Classify the preparation.
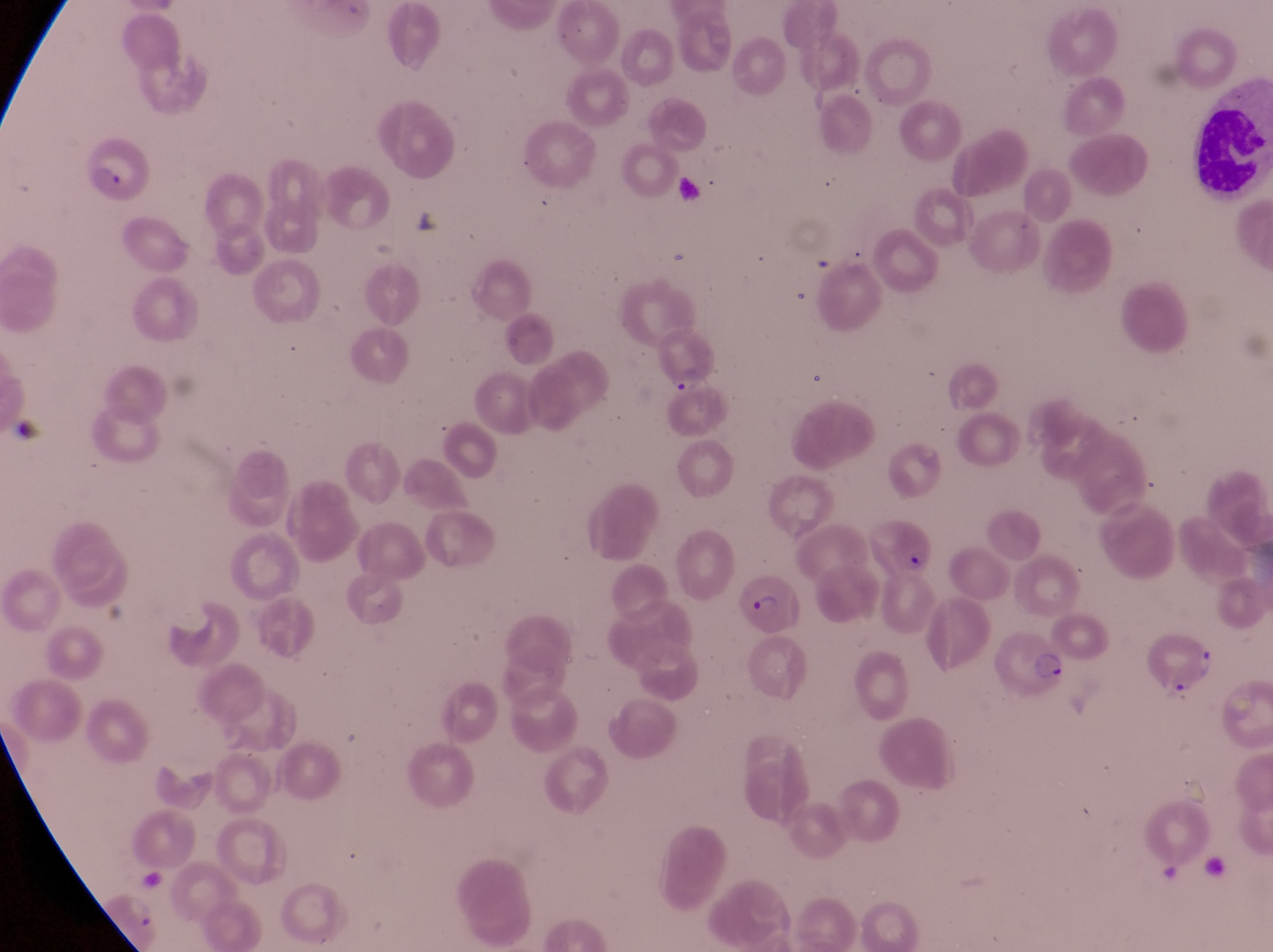
Thin blood smear.

Approximate bounding boxes as [left, top, right, bottom] in pixels.
Summary:
  - Leukocyte locations: [1190, 98, 1264, 196]
  - Artifact (platelet-like body, stain precipitate, or debris) locations: [405, 204, 444, 241], [12, 410, 49, 449]
  - Trophozoite locations: [666, 369, 708, 402]
  - Parasitised red blood cell locations: [78, 140, 152, 203], [870, 516, 935, 572], [732, 575, 801, 642], [993, 629, 1067, 696], [1146, 634, 1218, 701]
  - Field of view: single
  - Magnification: 1000x
  - Country: Uganda
  - Capture: smartphone photograph through the eyepiece of an Olympus CX-23 microscope
  - Image size: 1273×952 pixels